State which cell type is depicted.
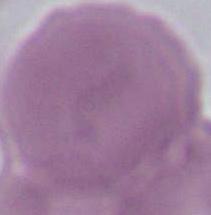
An erythrocyte.

magnification = 1000x
modality = photomicrograph